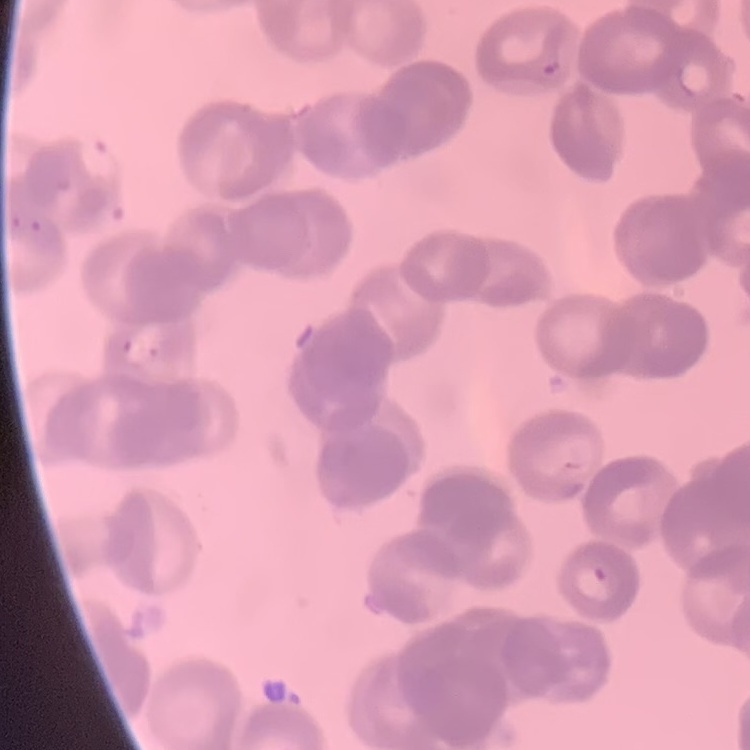
Summary:
  - Red blood cell morphology: rouleaux formation
  - Preparation: thin peripheral smear
  - Stain: Field's or Giemsa
  - Image type: square crop of a larger photomicrograph